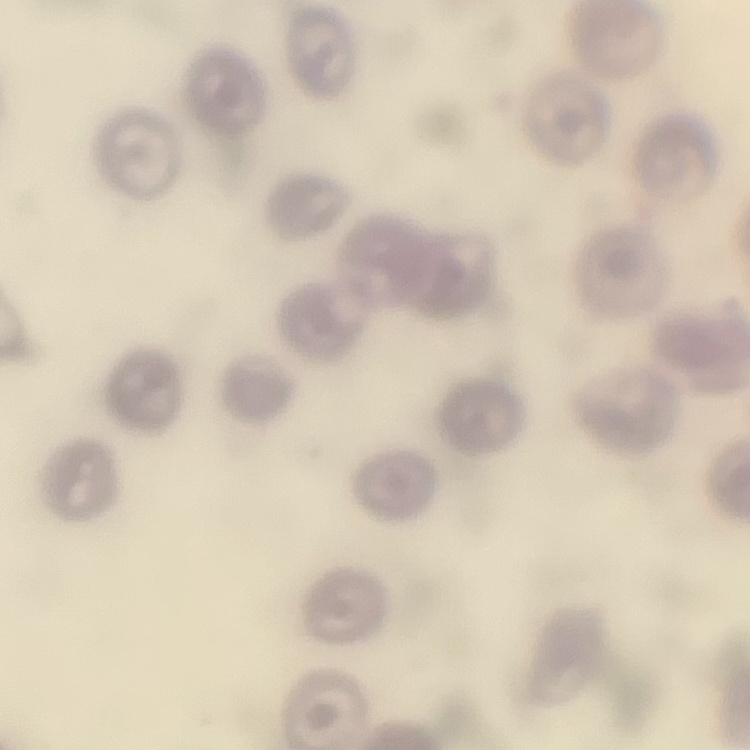
Summary:
  - Erythrocyte morphology: no rouleaux formation
  - Image type: square crop of a larger photomicrograph
  - Preparation: thin blood film
  - Stain: Field's or Giemsa